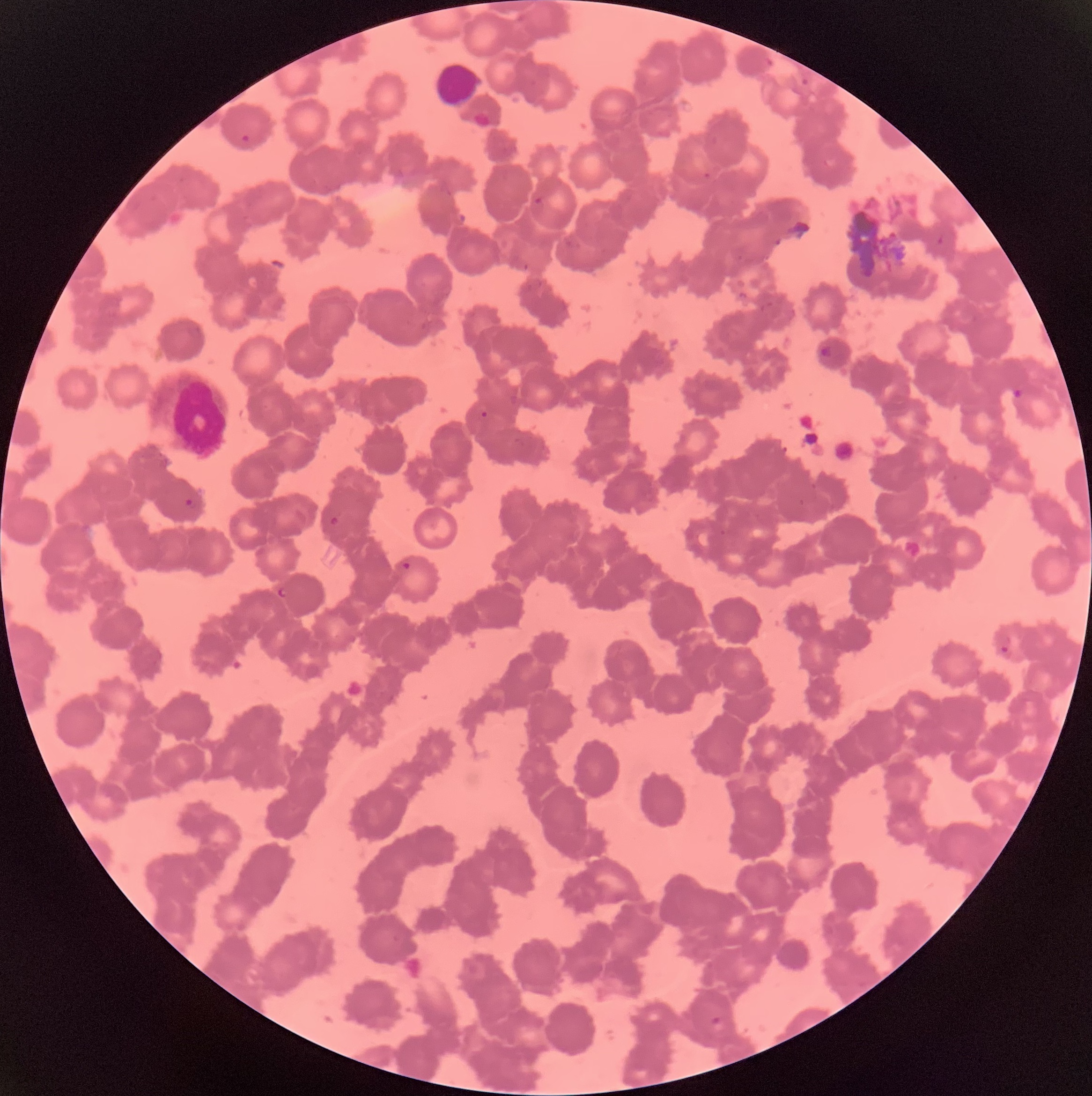
coordinate format = approximate bounding boxes as (x1,y1)-(x2,y2) corner pairs in pixels
Plasmodium parasite locations = (241,134)-(251,143), (818,346)-(831,357), (1009,385)-(1025,403), (185,497)-(196,510), (329,515)-(340,526), (277,587)-(290,599), (999,645)-(1012,657), (710,1015)-(723,1026)
Plasmodium parasites too small for a box (approximate centers as (x,y) in pixels) = (484,414)
white blood cell locations = (437,63)-(481,105)
red blood cell morphology = rouleaux formation
image size = 1092×1096 pixels
modality = light microscopy
preparation = thin blood film